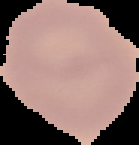
preparation: thin blood smear
result: negative for Plasmodium parasites
image_type: segmented cell region on a black background
image_size: 139×145 pixels